Mark where platelets are.
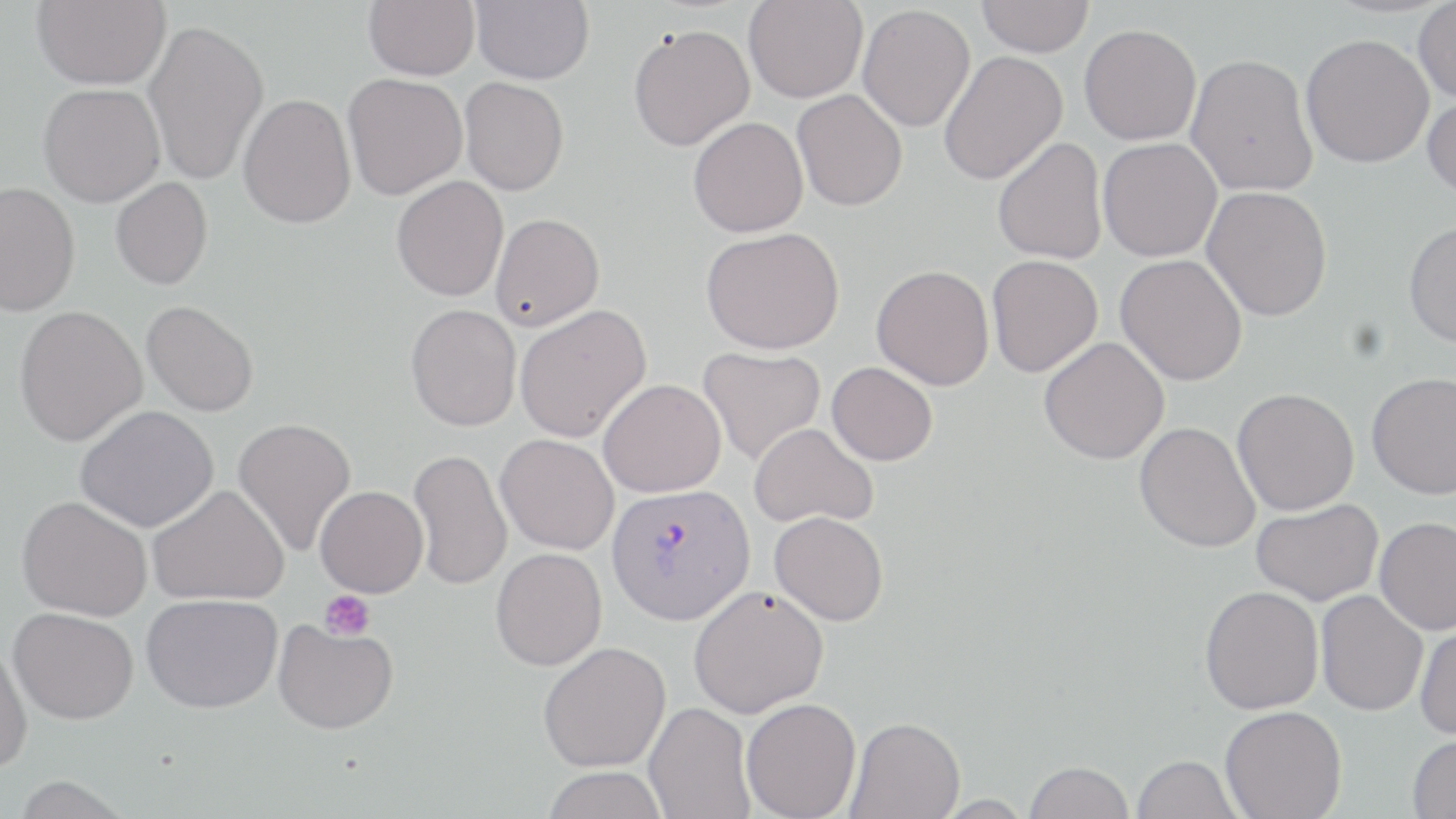

Approximate bounding boxes as [x1, y1, x2, y2] in pixels.
Platelets: [319, 590, 375, 641].

Uninfected red blood cell locations: [32, 0, 171, 89], [364, 0, 479, 80], [471, 0, 594, 84], [977, 0, 1094, 57], [743, 1, 868, 103], [1413, 1, 1456, 103], [857, 4, 975, 132], [142, 18, 269, 187], [628, 24, 755, 151], [1079, 24, 1201, 145], [1300, 33, 1434, 168], [939, 50, 1068, 186], [1185, 53, 1317, 196], [342, 72, 467, 200], [459, 77, 569, 195], [38, 83, 165, 207], [792, 89, 908, 211], [1422, 91, 1456, 201], [239, 93, 356, 229], [688, 117, 808, 237], [993, 137, 1108, 265], [1098, 138, 1222, 262], [391, 176, 509, 302], [111, 177, 213, 290], [0, 181, 80, 316], [1201, 185, 1333, 322], [491, 213, 605, 329], [1403, 219, 1456, 348], [701, 227, 844, 354], [1115, 254, 1248, 386], [986, 255, 1103, 377], [872, 265, 994, 390], [142, 300, 259, 417], [406, 304, 521, 431], [515, 304, 652, 443], [14, 305, 147, 447], [1038, 336, 1170, 465], [698, 346, 826, 466], [826, 362, 937, 466], [1366, 371, 1456, 499], [598, 379, 726, 497], [1233, 388, 1359, 515], [76, 405, 219, 532], [233, 417, 357, 557], [1134, 421, 1260, 553], [749, 422, 878, 528], [495, 434, 619, 554], [408, 447, 512, 590], [148, 484, 289, 606], [315, 485, 428, 597], [17, 496, 152, 621], [1251, 498, 1382, 606], [769, 511, 889, 626], [1375, 517, 1456, 635], [491, 547, 607, 670], [688, 585, 829, 718], [1200, 585, 1324, 714], [1315, 589, 1429, 716], [141, 593, 283, 713], [9, 607, 139, 724], [272, 619, 398, 735], [1414, 621, 1456, 741], [0, 640, 33, 775], [538, 641, 671, 772], [741, 697, 861, 819], [643, 701, 754, 819], [1220, 706, 1347, 819], [846, 716, 965, 819], [1407, 733, 1456, 819], [1131, 754, 1242, 818], [1023, 760, 1135, 819], [541, 766, 670, 819], [10, 776, 133, 818]. Plasmodium vivax-infected red blood cell locations: [606, 482, 754, 624]. Slide-level diagnosis: Plasmodium vivax. One field of a larger specimen. May-Grünwald-Giemsa stain. Captured at 1000x magnification. Image is 1456×819 pixels. Light microscopy. Thin blood smear.